Locate every uninfected red blood cell.
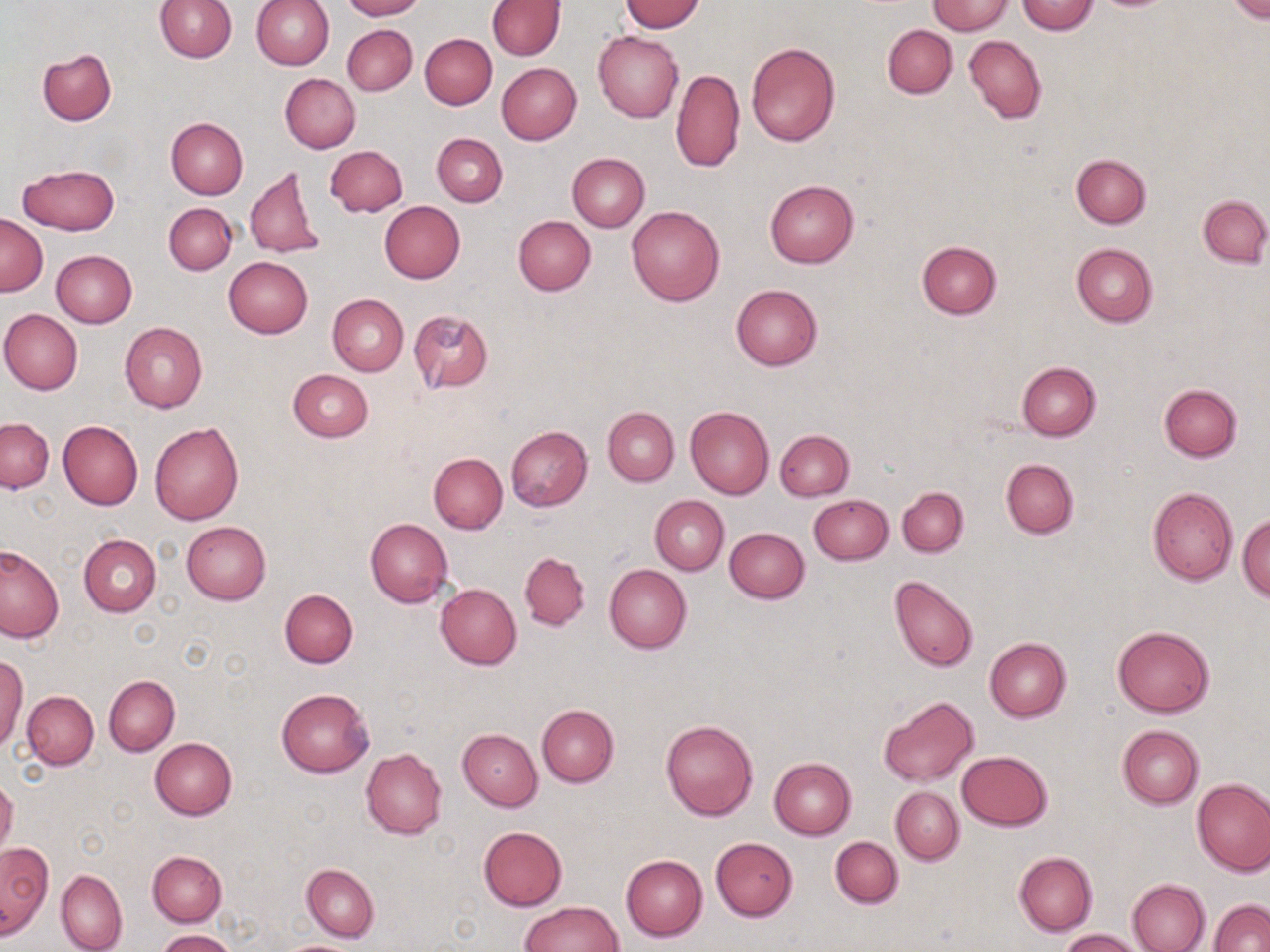

Approximate bounding boxes as [x1, y1, x2, y2] in pixels.
Uninfected red blood cells: [155, 0, 236, 62], [340, 0, 425, 20], [1226, 0, 1269, 23], [250, 1, 334, 69], [487, 1, 565, 60], [621, 1, 704, 32], [927, 1, 1013, 34], [1016, 1, 1099, 34], [342, 24, 416, 95], [882, 24, 956, 97], [593, 30, 683, 122], [419, 34, 496, 109], [964, 35, 1046, 123], [745, 41, 842, 147], [37, 48, 116, 126], [496, 63, 582, 145], [670, 67, 744, 174], [280, 74, 360, 153], [166, 117, 248, 198], [432, 133, 507, 206], [325, 146, 408, 216], [568, 153, 649, 232], [1071, 153, 1151, 228], [17, 163, 120, 235], [246, 166, 322, 261], [765, 179, 859, 267], [1198, 196, 1269, 267], [380, 201, 465, 282], [163, 202, 236, 275], [627, 206, 725, 307], [1, 214, 47, 296], [513, 215, 596, 295], [916, 240, 1002, 319], [1072, 242, 1158, 326], [51, 250, 136, 328], [223, 257, 312, 338], [731, 284, 822, 370], [328, 294, 408, 376], [0, 309, 83, 394], [406, 310, 494, 392], [120, 322, 207, 413], [1017, 362, 1101, 440], [287, 370, 373, 442], [1159, 383, 1244, 461], [685, 406, 774, 499], [603, 407, 678, 486], [1, 418, 54, 493], [58, 421, 143, 509], [149, 422, 243, 526], [506, 426, 593, 511], [774, 429, 854, 501], [428, 453, 507, 534], [1000, 458, 1079, 538], [897, 486, 968, 557], [1148, 488, 1238, 585], [649, 495, 729, 574], [808, 495, 893, 564], [1237, 514, 1269, 601], [366, 518, 452, 607], [181, 522, 270, 603], [724, 527, 809, 603], [79, 534, 162, 616], [0, 544, 65, 642], [520, 552, 590, 630], [604, 564, 691, 654], [889, 575, 977, 673], [435, 584, 522, 669], [280, 589, 357, 668], [1112, 625, 1214, 718], [985, 638, 1071, 722], [0, 656, 28, 752], [104, 675, 179, 756], [277, 688, 374, 777], [22, 690, 98, 769], [878, 695, 979, 788], [536, 705, 618, 788], [659, 718, 758, 821], [1117, 725, 1204, 808], [458, 728, 542, 810], [150, 737, 237, 819], [361, 748, 447, 838], [957, 751, 1053, 830], [769, 758, 857, 839], [0, 777, 18, 860], [1192, 779, 1270, 876], [891, 786, 964, 864], [478, 827, 567, 911], [830, 836, 903, 908], [711, 837, 798, 921], [0, 842, 52, 940], [147, 851, 226, 926], [1015, 851, 1098, 935], [620, 855, 707, 941], [302, 864, 379, 942], [56, 869, 127, 952], [1126, 878, 1211, 952], [1210, 899, 1270, 952], [519, 901, 621, 951], [1059, 928, 1147, 951], [156, 929, 235, 952], [274, 939, 367, 952].

Summary:
  - Slide-level diagnosis: negative for blood parasites
  - Field of view: single
  - Magnification: 1000x
  - Image size: 1270×952 pixels
  - Preparation: thin blood smear
  - Modality: optical microscopy
  - Stain: May-Grünwald-Giemsa